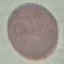
Summary:
  - Result: no malaria parasites detected
  - Stain: Giemsa
  - Capture: smartphone camera at the microscope eyepiece
  - Image type: automatically extracted cell patch, resized to 64 × 64 pixels
  - Preparation: thin blood film